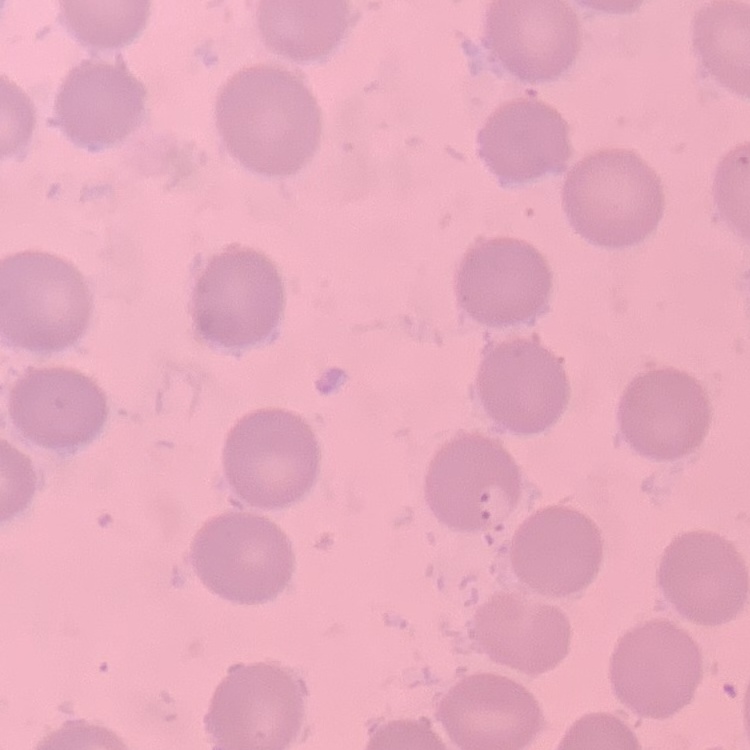
The red blood cells show no rouleaux formation. Square crop of a larger photomicrograph. Thin blood smear. Stained with either Field's or Giemsa.